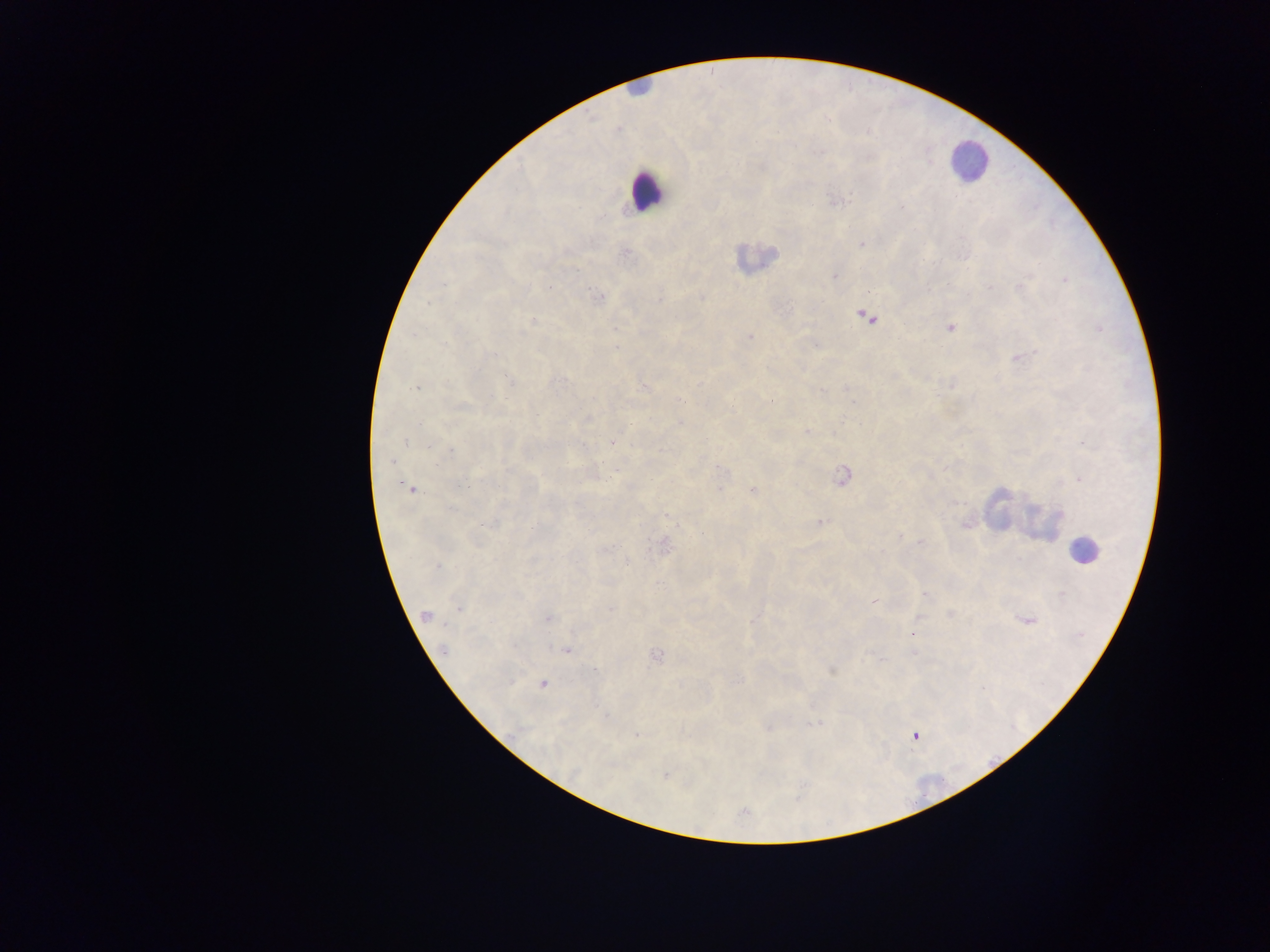
Approximate centers as x y in pixels. Malaria parasite locations: 838 200; 902 207; 861 244; 624 254; 576 270; 834 276; 1064 280; 441 284; 550 287; 990 287; 1019 287; 600 296; 702 298; 659 299; 867 317; 533 320; 950 328; 1099 329; 750 336; 616 348; 490 355; 1019 358; 509 382; 951 385; 644 387; 846 387; 417 388; 820 390; 682 401; 853 402; 462 404; 732 406; 588 419; 681 423; 807 432; 406 443; 613 443; 1084 445; 429 446; 581 446; 451 450; 392 461; 722 468; 508 469; 843 476; 1079 479; 410 489; 719 490; 753 491; 450 509; 667 516; 820 522; 966 523; 490 524; 900 536; 921 542; 664 546; 606 548; 626 563; 437 566; 924 594; 1061 594; 874 601; 459 608; 611 608; 426 615; 950 615; 548 619; 917 619; 1027 620; 913 631; 442 650; 567 650; 913 652; 656 655; 594 670; 832 670; 543 683; 982 689; 605 715; 815 724; 768 728; 637 736; 915 736; 575 773; 665 776. Leukocyte locations: 968 161; 647 191; 755 257; 1018 515; 1040 522; 1086 551. Single field of view. Sample from Ghana. Mobile-phone photograph taken through the microscope. Image is 1270×952 pixels. Thick blood film.